Classify this cell by malaria status.
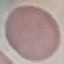
It is uninfected.

Automatically extracted cell patch, resized to 64 × 64 pixels. Acquired by smartphone through the microscope eyepiece. Thin blood film. Giemsa stain.